Name the cell type shown.
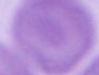
An erythrocyte.

modality = photomicrograph
magnification = 1000x